Assess the morphology of the red blood cells.
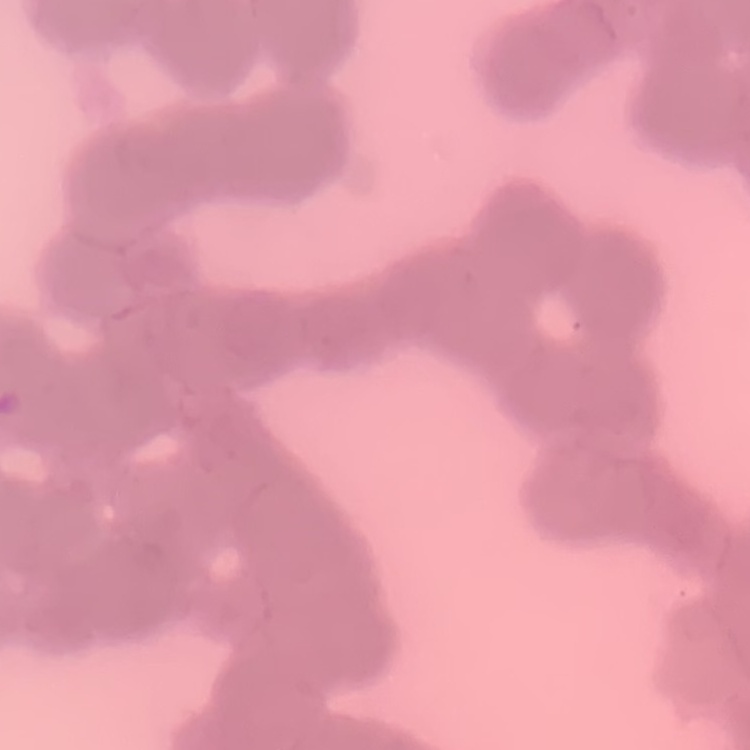
Rouleaux formation.

{
  "image_type": "one tile cut from a larger photomicrograph",
  "preparation": "thin blood smear",
  "stain": "Field's or Giemsa"
}